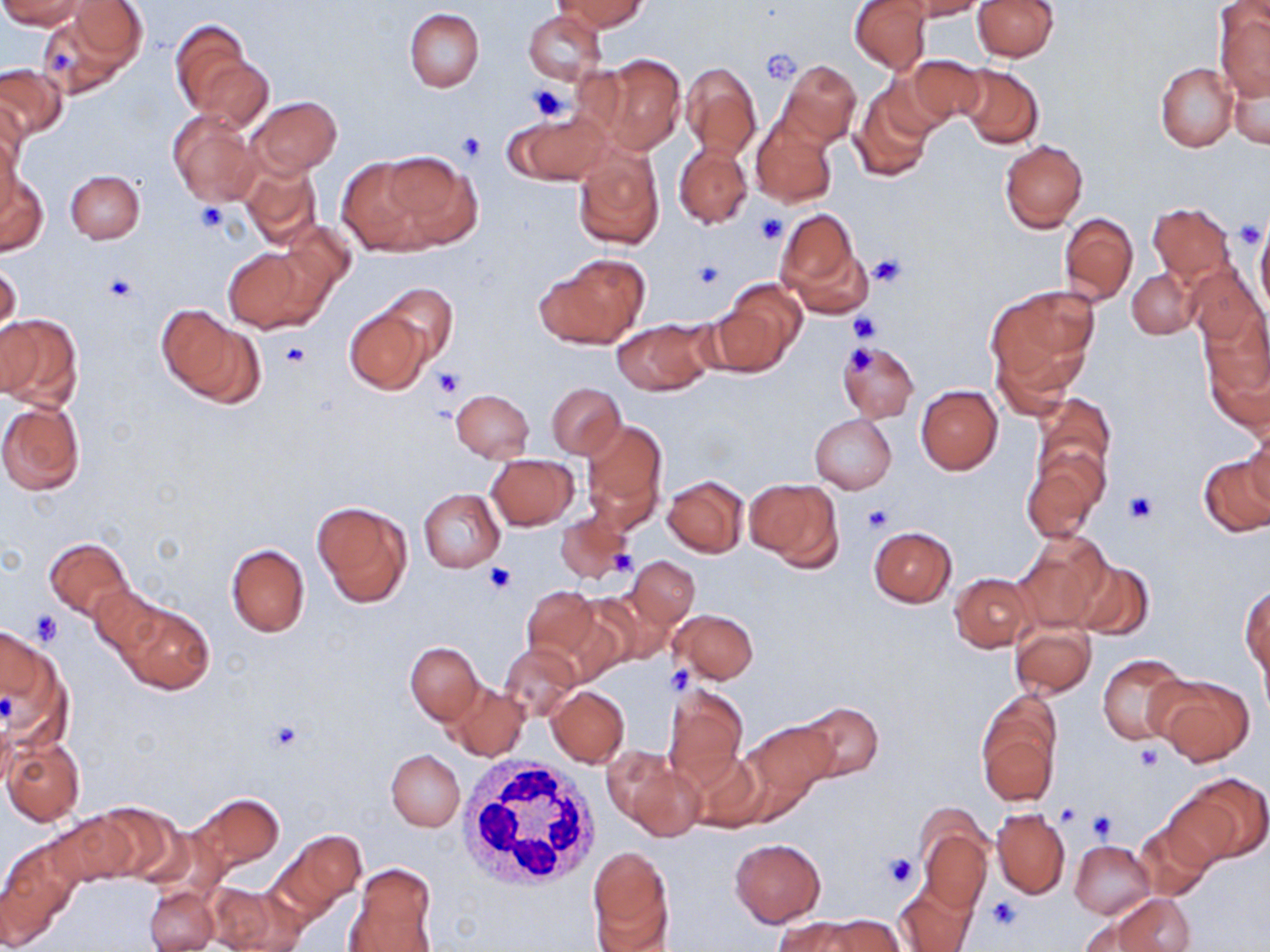

Approximate bounding boxes as (x1, y1, x2, y2) in pixels. Platelet locations: (760, 49, 802, 83), (527, 81, 572, 122), (457, 131, 488, 162), (196, 202, 227, 234), (755, 213, 787, 245), (1235, 220, 1264, 249), (868, 251, 907, 289), (693, 260, 727, 288), (103, 275, 140, 302), (846, 313, 880, 344), (283, 341, 310, 367), (844, 342, 881, 377), (432, 366, 464, 400), (1124, 489, 1158, 524), (862, 504, 892, 532), (484, 563, 518, 594), (30, 610, 63, 647), (665, 666, 693, 693), (266, 719, 306, 752), (1134, 742, 1162, 771), (1054, 803, 1080, 825), (1086, 810, 1116, 841), (882, 852, 920, 888), (986, 897, 1021, 930). White blood cell locations: (458, 753, 604, 891). Uninfected red blood cell locations: (1, 0, 91, 29), (555, 0, 646, 34), (850, 0, 931, 74), (912, 0, 986, 20), (972, 0, 1058, 61), (42, 5, 141, 96), (1216, 7, 1269, 101), (405, 8, 484, 91), (525, 11, 604, 84), (170, 22, 261, 123), (585, 54, 688, 153), (190, 55, 273, 133), (902, 55, 986, 129), (777, 59, 861, 148), (0, 62, 67, 143), (1155, 62, 1238, 152), (680, 63, 761, 161), (955, 64, 1044, 149), (1228, 67, 1270, 150), (851, 85, 936, 182), (248, 97, 342, 177), (167, 110, 262, 207), (505, 111, 614, 185), (752, 113, 837, 208), (1, 122, 22, 217), (999, 140, 1088, 233), (573, 143, 664, 249), (674, 144, 753, 228), (380, 151, 481, 250), (240, 156, 323, 249), (337, 156, 438, 254), (65, 170, 144, 244), (1, 171, 47, 255), (1149, 202, 1237, 289), (774, 209, 870, 317), (1059, 211, 1138, 306), (276, 219, 359, 302), (1256, 225, 1270, 315), (222, 245, 327, 333), (534, 256, 650, 350), (0, 262, 21, 337), (1185, 265, 1266, 347), (1127, 269, 1197, 338), (712, 281, 804, 372), (377, 283, 458, 365), (985, 284, 1100, 394), (343, 308, 431, 395), (159, 309, 262, 405), (0, 313, 82, 410), (1199, 314, 1270, 429), (612, 319, 714, 396), (837, 341, 919, 423), (991, 345, 1076, 421), (546, 382, 625, 459), (915, 385, 1002, 474), (450, 389, 534, 461), (1030, 395, 1115, 505), (0, 400, 85, 494), (810, 414, 896, 494), (1245, 416, 1270, 506), (579, 418, 666, 532), (1023, 448, 1107, 542), (1200, 454, 1270, 536), (488, 455, 579, 530), (663, 475, 748, 556), (745, 477, 843, 572), (418, 489, 505, 572), (313, 500, 411, 608), (553, 511, 634, 585), (868, 526, 957, 606), (1014, 532, 1109, 631), (44, 537, 133, 620), (226, 543, 310, 636), (627, 556, 699, 631), (1072, 559, 1154, 642), (950, 572, 1035, 652), (519, 584, 604, 672), (90, 587, 168, 665), (1241, 587, 1269, 680), (113, 600, 215, 695), (669, 610, 757, 683), (1011, 624, 1095, 698), (0, 628, 47, 705), (406, 642, 482, 724), (500, 645, 580, 721), (1098, 654, 1188, 744), (1148, 673, 1255, 766), (448, 683, 529, 761), (663, 684, 748, 786), (547, 686, 629, 767), (795, 701, 883, 781), (979, 717, 1058, 807), (739, 720, 839, 817), (3, 738, 83, 826), (385, 749, 464, 831), (604, 749, 703, 841), (688, 749, 767, 832), (1184, 775, 1269, 863), (191, 792, 284, 873), (1160, 794, 1241, 871), (89, 802, 184, 884), (992, 809, 1070, 898), (48, 812, 139, 887), (1135, 820, 1215, 900), (918, 821, 991, 913), (268, 831, 366, 923), (729, 838, 826, 928), (1070, 840, 1155, 918), (2, 848, 77, 949), (587, 849, 675, 950), (346, 862, 437, 951), (204, 882, 292, 951), (893, 882, 977, 952), (145, 887, 217, 952), (1110, 894, 1195, 952), (815, 915, 903, 952), (774, 916, 867, 952). Slide-level diagnosis: negative for blood parasites. Thin blood film. One field of a larger specimen. Captured at 1000x magnification. May-Grünwald-Giemsa-stained preparation. Light microscopy. Image is 1270×952 pixels.